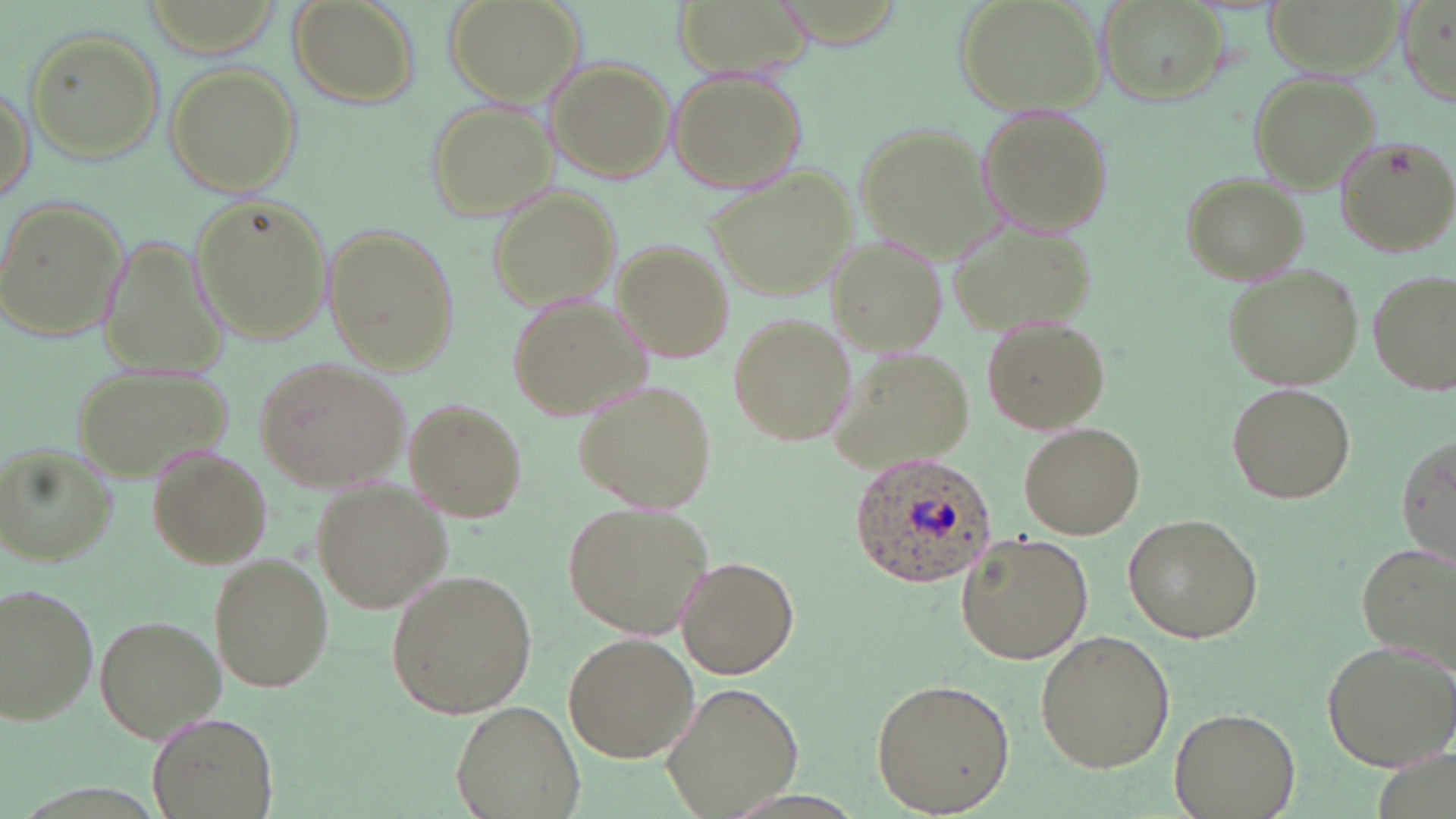

slide-level diagnosis = Plasmodium ovale
stain = May-Grünwald-Giemsa
field of view = one of a larger specimen
modality = light microscopy
magnification = 1000x
Plasmodium ovale-infected red blood cell locations = approximate bounding boxes as [x1, y1, x2, y2] in pixels: [847, 452, 996, 587]
uninfected red blood cell locations = approximate bounding boxes as [x1, y1, x2, y2] in pixels: [446, 0, 587, 108], [671, 0, 811, 72], [956, 0, 1104, 120], [1094, 0, 1229, 105], [1262, 0, 1401, 75], [288, 1, 419, 111], [1398, 2, 1456, 108], [24, 27, 165, 164], [546, 58, 675, 183], [164, 61, 300, 195], [668, 69, 807, 194], [1250, 72, 1380, 192], [1, 79, 34, 203], [424, 99, 553, 220], [977, 108, 1117, 242], [852, 121, 1000, 256], [1335, 136, 1455, 256], [707, 170, 856, 298], [1180, 171, 1307, 284], [489, 188, 623, 311], [191, 193, 336, 344], [0, 198, 131, 343], [947, 215, 1097, 341], [322, 226, 457, 373], [824, 236, 949, 351], [610, 240, 736, 361], [1220, 262, 1364, 392], [1369, 270, 1456, 397], [505, 293, 652, 423], [726, 312, 856, 446], [981, 317, 1109, 435], [822, 345, 974, 475], [252, 357, 411, 493], [70, 362, 231, 478], [575, 380, 717, 514], [1225, 381, 1356, 505], [404, 400, 527, 523], [1019, 421, 1147, 538], [1394, 431, 1456, 570], [1, 443, 114, 567], [149, 450, 272, 569], [315, 479, 450, 612], [561, 498, 714, 643], [1124, 515, 1261, 644], [955, 531, 1094, 665], [1358, 539, 1454, 673], [677, 555, 800, 680], [210, 556, 332, 692], [386, 569, 537, 720], [1, 583, 99, 729], [94, 614, 225, 741], [1034, 629, 1175, 772], [562, 632, 698, 763], [1320, 636, 1456, 769], [870, 676, 1016, 815], [660, 679, 806, 817], [452, 700, 587, 819], [1170, 706, 1299, 819], [146, 712, 275, 818]
image size = 1456×819 pixels
preparation = thin blood smear